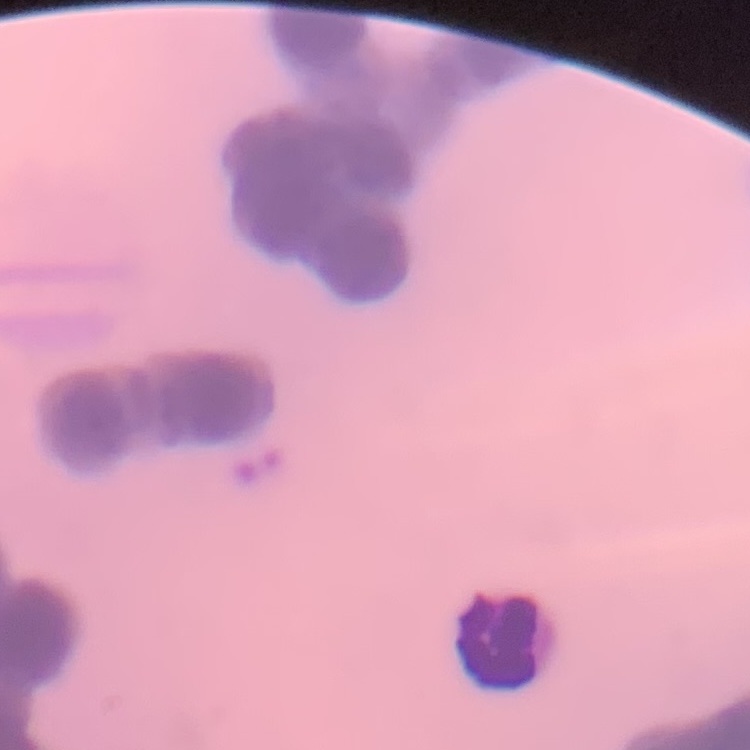 The erythrocytes exhibit rouleaux formation. Stained with either Field's or Giemsa. Square crop of a larger photomicrograph. Thin blood film.